Classify this cell by malaria status.
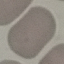
It is uninfected.

Summary:
  - Image type: cell patch, automatically extracted from a larger field of view and resized to 64 × 64 pixels
  - Capture: smartphone camera at the microscope eyepiece
  - Stain: Giemsa
  - Preparation: thin blood smear